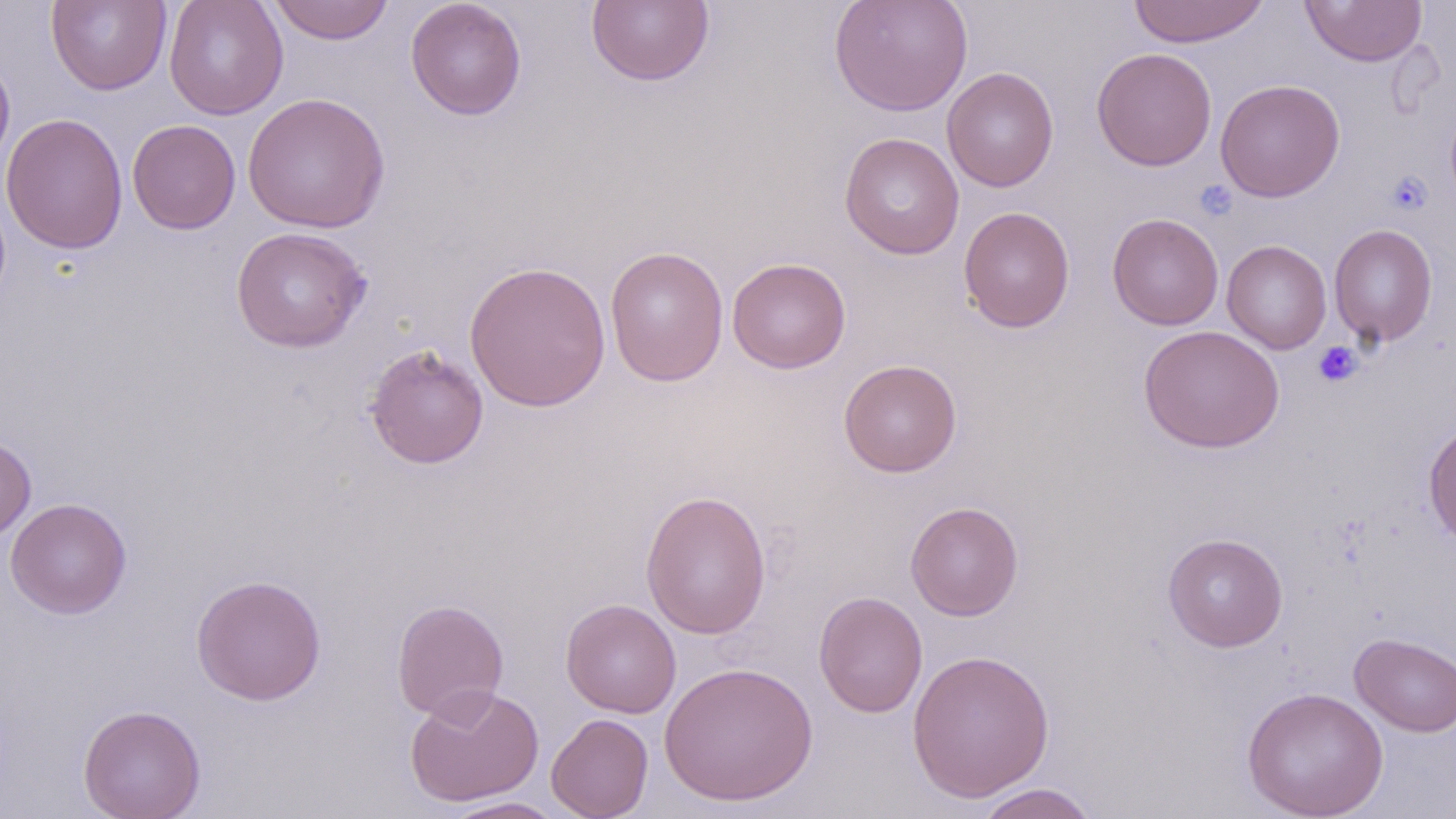

{
  "slide_level_diagnosis": "negative for blood parasites",
  "uninfected_red_blood_cell_locations": "approximate bounding boxes as named x1/y1/x2/y2 corners in pixels: (x1=46, y1=0, x2=172, y2=96), (x1=164, y1=0, x2=289, y2=120), (x1=267, y1=0, x2=395, y2=45), (x1=406, y1=0, x2=527, y2=120), (x1=585, y1=0, x2=715, y2=88), (x1=828, y1=0, x2=973, y2=117), (x1=1127, y1=0, x2=1270, y2=48), (x1=1299, y1=0, x2=1427, y2=67), (x1=1091, y1=47, x2=1217, y2=171), (x1=0, y1=50, x2=16, y2=181), (x1=942, y1=67, x2=1059, y2=192), (x1=1215, y1=79, x2=1345, y2=202), (x1=242, y1=93, x2=392, y2=233), (x1=1, y1=113, x2=128, y2=254), (x1=127, y1=119, x2=241, y2=234), (x1=839, y1=132, x2=965, y2=259), (x1=958, y1=206, x2=1075, y2=332), (x1=1106, y1=212, x2=1224, y2=331), (x1=1328, y1=223, x2=1438, y2=347), (x1=231, y1=227, x2=371, y2=352), (x1=1221, y1=239, x2=1332, y2=354), (x1=605, y1=245, x2=729, y2=386), (x1=727, y1=257, x2=851, y2=374), (x1=464, y1=260, x2=612, y2=413), (x1=1138, y1=324, x2=1285, y2=453), (x1=363, y1=343, x2=490, y2=470), (x1=838, y1=359, x2=962, y2=478), (x1=1423, y1=420, x2=1456, y2=550), (x1=0, y1=434, x2=37, y2=543), (x1=640, y1=488, x2=772, y2=640), (x1=5, y1=498, x2=132, y2=619), (x1=905, y1=501, x2=1023, y2=621), (x1=1162, y1=532, x2=1289, y2=652), (x1=191, y1=573, x2=326, y2=706), (x1=813, y1=591, x2=928, y2=718), (x1=391, y1=598, x2=509, y2=722), (x1=560, y1=598, x2=682, y2=718), (x1=1350, y1=633, x2=1456, y2=737), (x1=906, y1=649, x2=1056, y2=803), (x1=659, y1=660, x2=819, y2=807), (x1=404, y1=684, x2=544, y2=807), (x1=1240, y1=686, x2=1389, y2=819), (x1=78, y1=704, x2=206, y2=819), (x1=546, y1=713, x2=654, y2=819), (x1=972, y1=783, x2=1102, y2=819), (x1=438, y1=796, x2=570, y2=818)",
  "stain": "May-Grünwald-Giemsa",
  "modality": "light microscopy",
  "magnification": "1000x",
  "image_size": "1456×819 pixels",
  "field_of_view": "single",
  "platelet_locations": "approximate bounding boxes as named x1/y1/x2/y2 corners in pixels: (x1=1386, y1=171, x2=1431, y2=215), (x1=1196, y1=180, x2=1236, y2=220), (x1=1313, y1=341, x2=1363, y2=387)",
  "preparation": "thin blood smear"
}